Assess this cell for malaria.
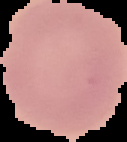
It is uninfected.

From a thin blood film. Image is 127×142 pixels. The area outside the segmented cell region is set to black.